Locate every Plasmodium malariae-infected red blood cell.
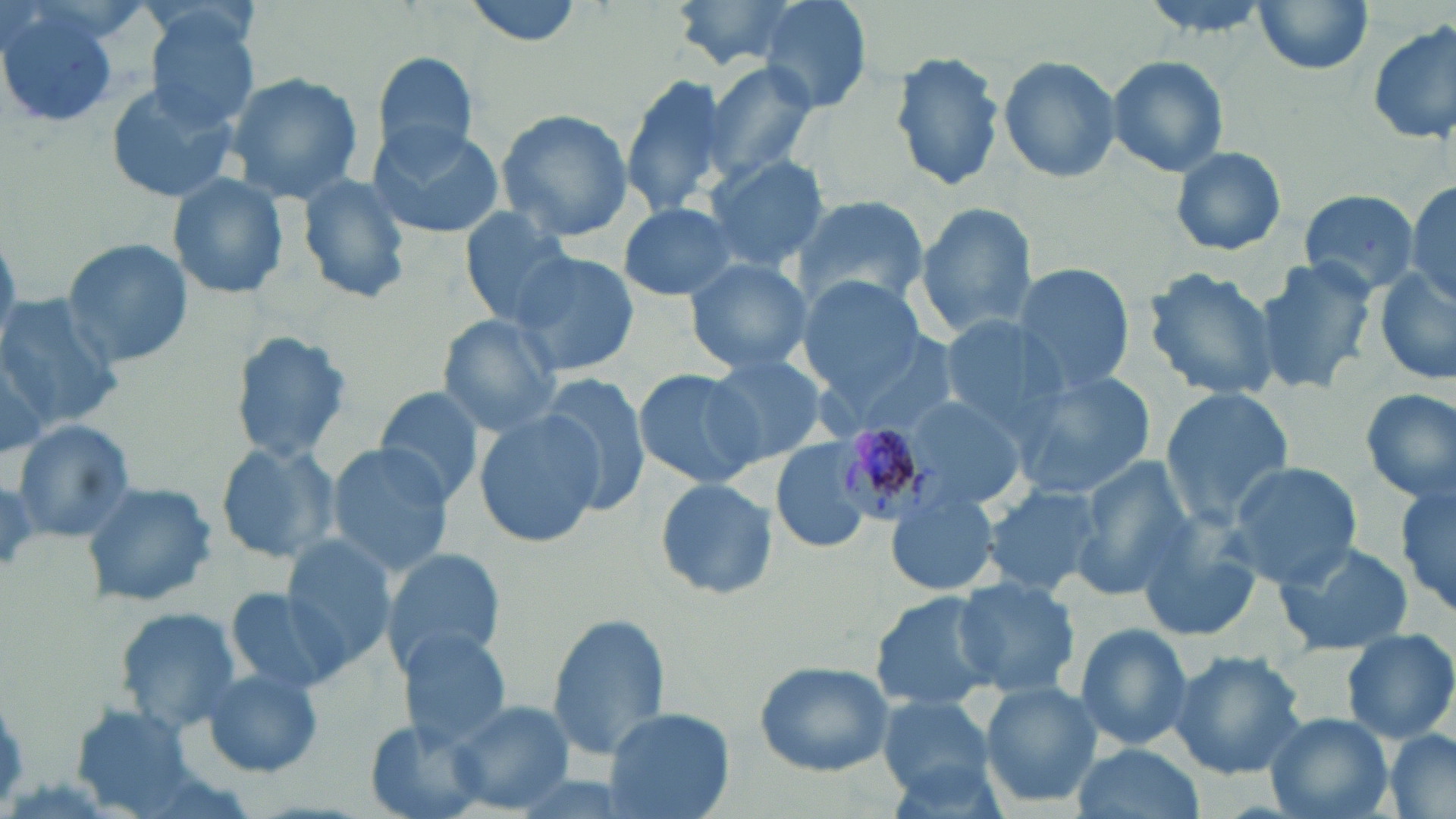
Approximate bounding boxes as [x1, y1, x2, y2] in pixels.
Plasmodium malariae-infected red blood cells: [825, 420, 953, 526].

Uninfected red blood cell locations: [460, 0, 591, 47], [754, 0, 874, 114], [671, 1, 805, 70], [1248, 1, 1376, 74], [0, 3, 119, 131], [141, 5, 266, 130], [1367, 19, 1455, 147], [889, 48, 1007, 193], [366, 51, 483, 167], [996, 55, 1120, 184], [1105, 55, 1229, 177], [697, 61, 821, 183], [223, 71, 365, 207], [621, 73, 730, 215], [103, 80, 240, 205], [496, 109, 634, 244], [366, 121, 505, 240], [1169, 144, 1289, 257], [701, 153, 830, 273], [171, 173, 289, 299], [296, 173, 412, 305], [1403, 182, 1455, 306], [1297, 188, 1421, 296], [791, 195, 930, 316], [618, 201, 742, 301], [914, 202, 1041, 340], [457, 210, 584, 327], [60, 237, 190, 370], [508, 251, 640, 380], [683, 256, 812, 376], [1254, 259, 1378, 396], [1011, 262, 1136, 394], [1142, 268, 1282, 403], [1373, 270, 1456, 384], [799, 275, 927, 397], [0, 294, 122, 431], [437, 316, 564, 436], [935, 318, 1070, 431], [824, 328, 960, 442], [229, 331, 354, 463], [0, 342, 53, 456], [701, 352, 833, 462], [632, 367, 768, 490], [1009, 369, 1157, 499], [539, 374, 652, 514], [1359, 386, 1456, 503], [1159, 387, 1294, 525], [374, 388, 484, 505], [898, 392, 1033, 511], [474, 409, 603, 546], [10, 419, 137, 543], [768, 438, 877, 556], [215, 440, 339, 564], [327, 443, 455, 576], [1070, 456, 1198, 595], [1226, 461, 1362, 585], [652, 477, 778, 601], [1394, 477, 1455, 619], [79, 480, 217, 608], [981, 484, 1103, 596], [883, 485, 998, 599], [1135, 526, 1259, 643], [279, 537, 399, 669], [1273, 539, 1414, 655], [382, 547, 509, 676], [950, 576, 1083, 697], [223, 587, 347, 695], [868, 591, 1001, 714], [114, 605, 244, 732], [547, 612, 671, 763], [1072, 622, 1195, 755], [397, 628, 514, 747], [1340, 629, 1456, 745], [1170, 650, 1307, 778], [754, 658, 895, 776], [199, 666, 325, 778], [979, 681, 1103, 809], [880, 697, 998, 801], [444, 698, 575, 814], [72, 706, 198, 815], [602, 706, 734, 819], [1265, 712, 1394, 819], [359, 721, 488, 818], [1381, 730, 1456, 819], [1069, 742, 1203, 819]. Slide-level diagnosis: Plasmodium malariae. Thin blood smear. Image is 1456×819 pixels. May-Grünwald-Giemsa-stained preparation. One field of a larger specimen. Captured at 1000x magnification. Light microscopy.